Report the malaria status of this cell.
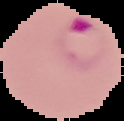
Parasitized.

Summary:
  - Image type: cell region segmented out of the field of view; surrounding area masked to black
  - Image size: 124×121 pixels
  - Preparation: thin blood film